Identify the parasite.
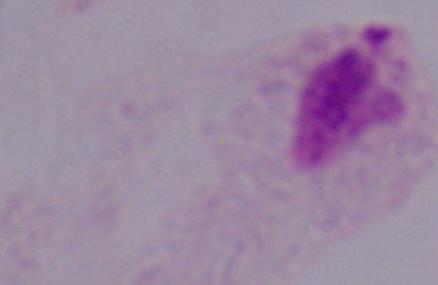

This is a trichomonad.

Captured at 1000x magnification. Micrograph.